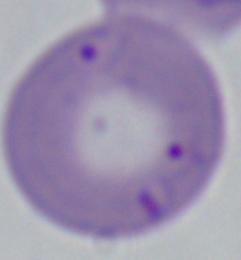
Summary:
  - Modality: photomicrograph
  - Identification: Babesia
  - Magnification: 1000x